Name the parasite shown.
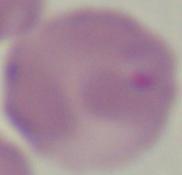

This is Babesia.

Summary:
  - Magnification: 1000x
  - Modality: photomicrograph